Assess the morphology of the erythrocytes.
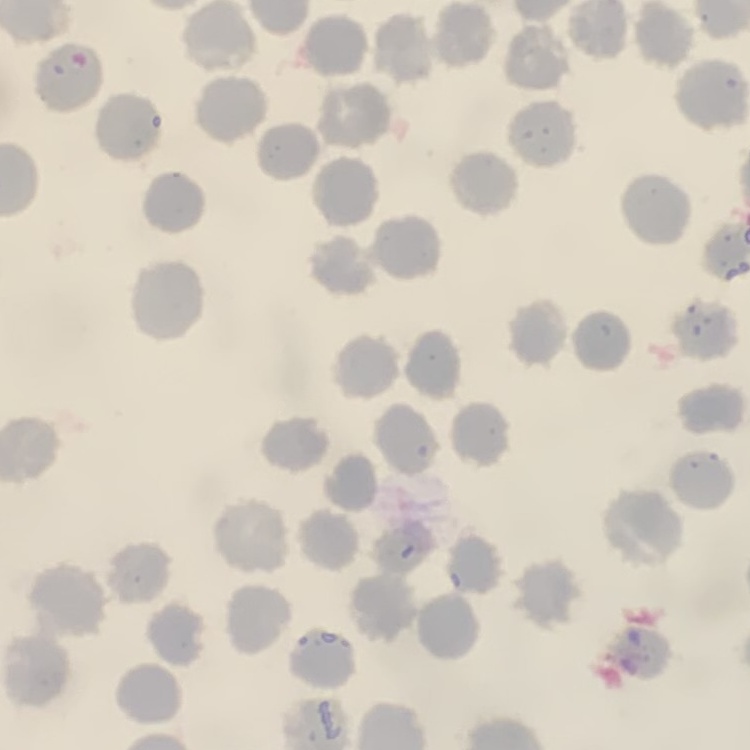

No rouleaux formation.

Summary:
  - Stain: Field's or Giemsa
  - Image type: square crop of a larger photomicrograph
  - Preparation: thin blood smear